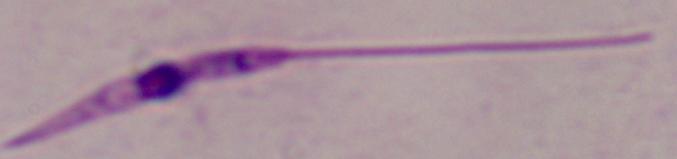
Photomicrograph. 1000x magnification. A Leishmania parasite is shown.